State the blood parasite species.
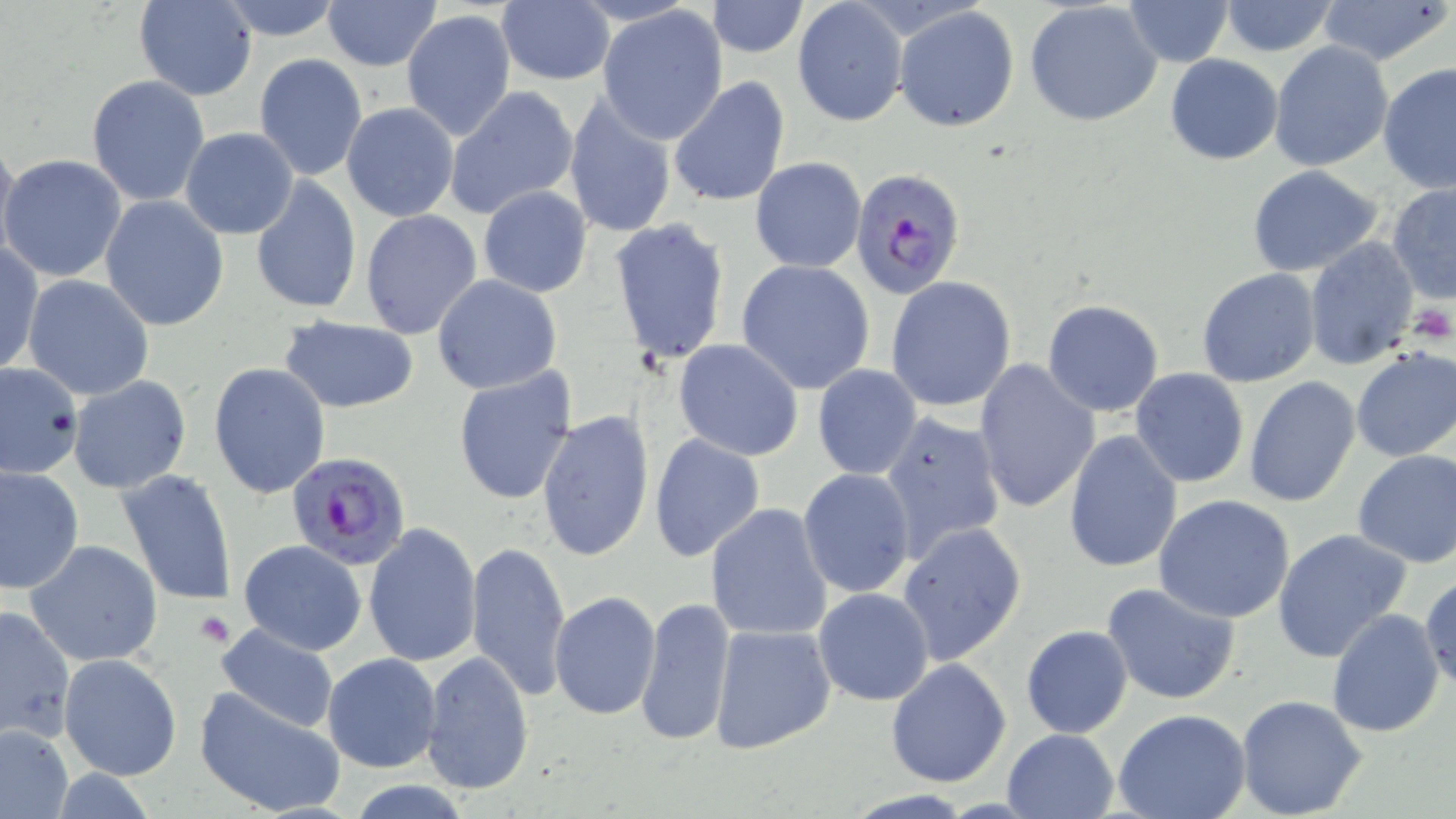

Plasmodium falciparum.

uninfected red blood cell locations = approximate bounding boxes as (x1,y1)-(x2,y2) corner pairs in pixels: (134,0)-(256,100), (210,0)-(348,41), (321,0)-(442,70), (1122,0)-(1234,68), (1315,0)-(1455,66), (1024,1)-(1162,126), (1218,1)-(1339,56), (496,2)-(615,86), (705,2)-(809,58), (793,2)-(907,127), (597,6)-(729,143), (893,6)-(1020,131), (402,10)-(516,141), (1269,41)-(1395,173), (1165,53)-(1283,165), (254,54)-(367,181), (1378,62)-(1456,196), (86,74)-(211,206), (668,75)-(790,211), (446,86)-(578,218), (562,95)-(677,238), (341,102)-(460,223), (180,127)-(299,240), (0,137)-(19,262), (1,153)-(127,282), (750,156)-(866,273), (1246,165)-(1386,277), (250,175)-(362,316), (1386,182)-(1455,306), (478,186)-(592,298), (99,196)-(229,332), (454,202)-(583,358), (360,209)-(484,341), (608,218)-(731,365), (1304,237)-(1418,369), (0,242)-(43,376), (737,259)-(876,393), (1197,267)-(1322,388), (23,274)-(155,400), (432,275)-(563,395), (886,276)-(1018,412), (1042,299)-(1165,416), (277,318)-(421,413), (673,339)-(804,461), (1350,349)-(1456,463), (973,358)-(1099,515), (0,362)-(82,479), (209,362)-(331,499), (812,364)-(921,479), (1130,368)-(1249,489), (452,369)-(577,505), (68,376)-(193,494), (1243,377)-(1359,507), (537,410)-(655,559), (877,410)-(1008,561), (1063,430)-(1183,574), (649,434)-(766,563), (1351,450)-(1456,567), (1,467)-(84,595), (116,468)-(239,607), (798,469)-(916,598), (1153,494)-(1295,622), (705,502)-(834,642), (363,521)-(481,667), (897,523)-(1027,665), (1271,528)-(1413,664), (26,539)-(164,668), (238,539)-(367,655), (466,540)-(570,703), (1419,576)-(1455,691), (1102,581)-(1242,704), (813,588)-(934,706), (550,592)-(661,721), (634,596)-(736,747), (0,604)-(75,744), (1325,608)-(1445,738), (214,622)-(341,734), (708,623)-(837,753), (1021,625)-(1133,740), (420,649)-(535,796), (322,652)-(442,774), (59,653)-(181,778), (886,659)-(1012,788), (193,687)-(346,819), (1236,695)-(1368,819), (1114,710)-(1251,819), (1,724)-(71,819), (1000,728)-(1120,819)
Plasmodium falciparum-infected red blood cell locations = approximate bounding boxes as (x1,y1)-(x2,y2) corner pairs in pixels: (848,166)-(966,299), (286,451)-(413,571)
preparation = thin blood film
field of view = one of a larger specimen
stain = May-Grünwald-Giemsa
platelet locations = approximate bounding boxes as (x1,y1)-(x2,y2) corner pairs in pixels: (1407,304)-(1453,343), (194,609)-(234,646)
magnification = 1000x
image size = 1456×819 pixels
modality = light microscopy